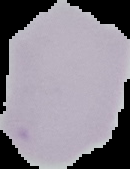
Summary:
  - Result: negative for malaria parasites
  - Image size: 130×169 pixels
  - Preparation: thin blood film
  - Image type: segmented cell region on a black background